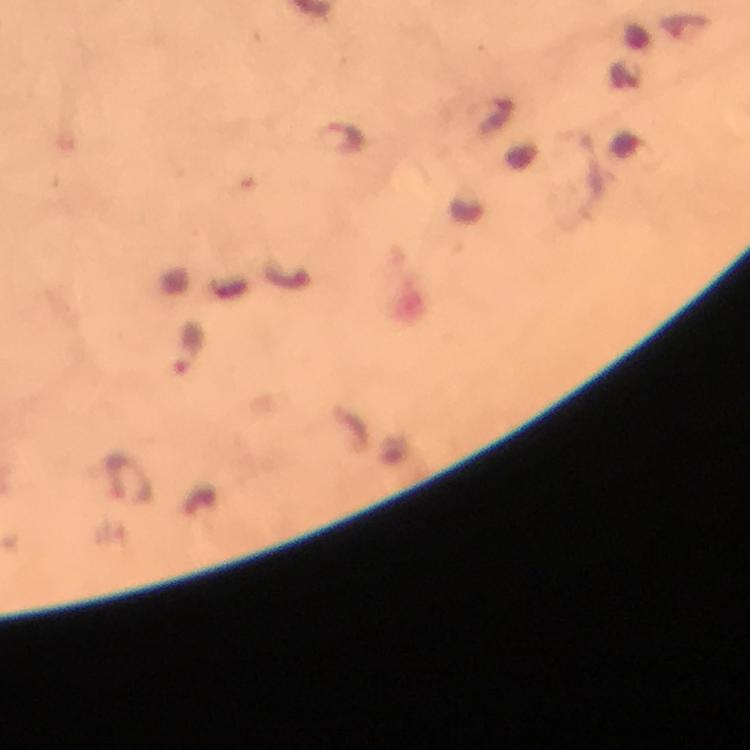
Approximate centers as {x, y} in pixels. Plasmodium parasite locations: {337, 139}, {187, 350}. Cropped region of a single field of view. Immersion oil was used. Photographed through the microscope with a smartphone camera. Giemsa stain. At 100x magnification. From a malaria diagnostic workup. Image is 750×750 pixels. Thick smear.